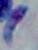
magnification = 1000x
identification = Toxoplasma gondii
modality = micrograph